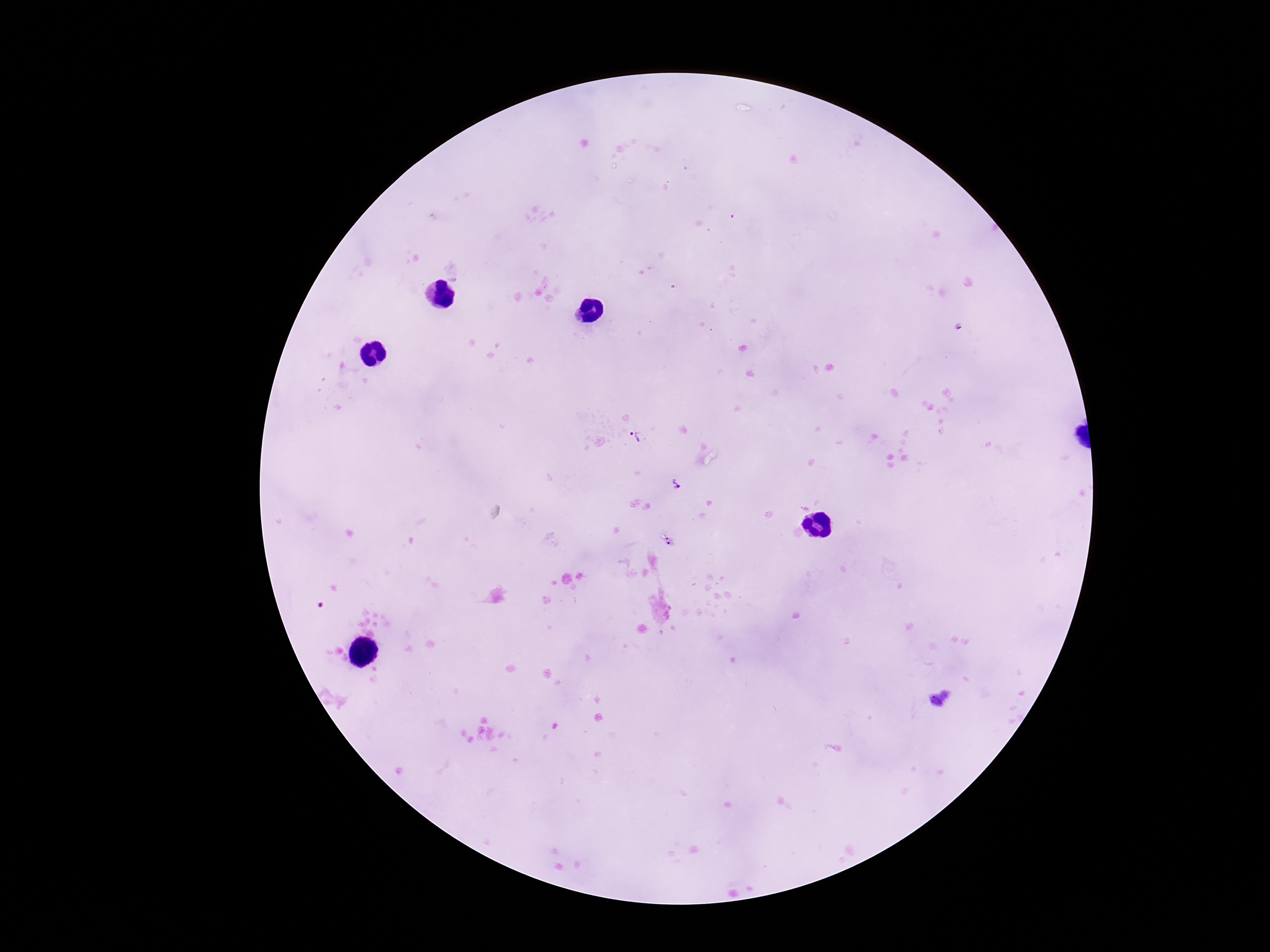

Approximate centers as {x, y} in pixels.
Summary:
  - Plasmodium parasite locations: {637, 437}, {678, 484}, {669, 542}
  - Stain: Giemsa
  - Capture: smartphone camera through the microscope eyepiece
  - Patient malaria status: infected
  - Field of view: single
  - Magnification: 100x
  - Preparation: thick blood film
  - Image size: 1270×952 pixels